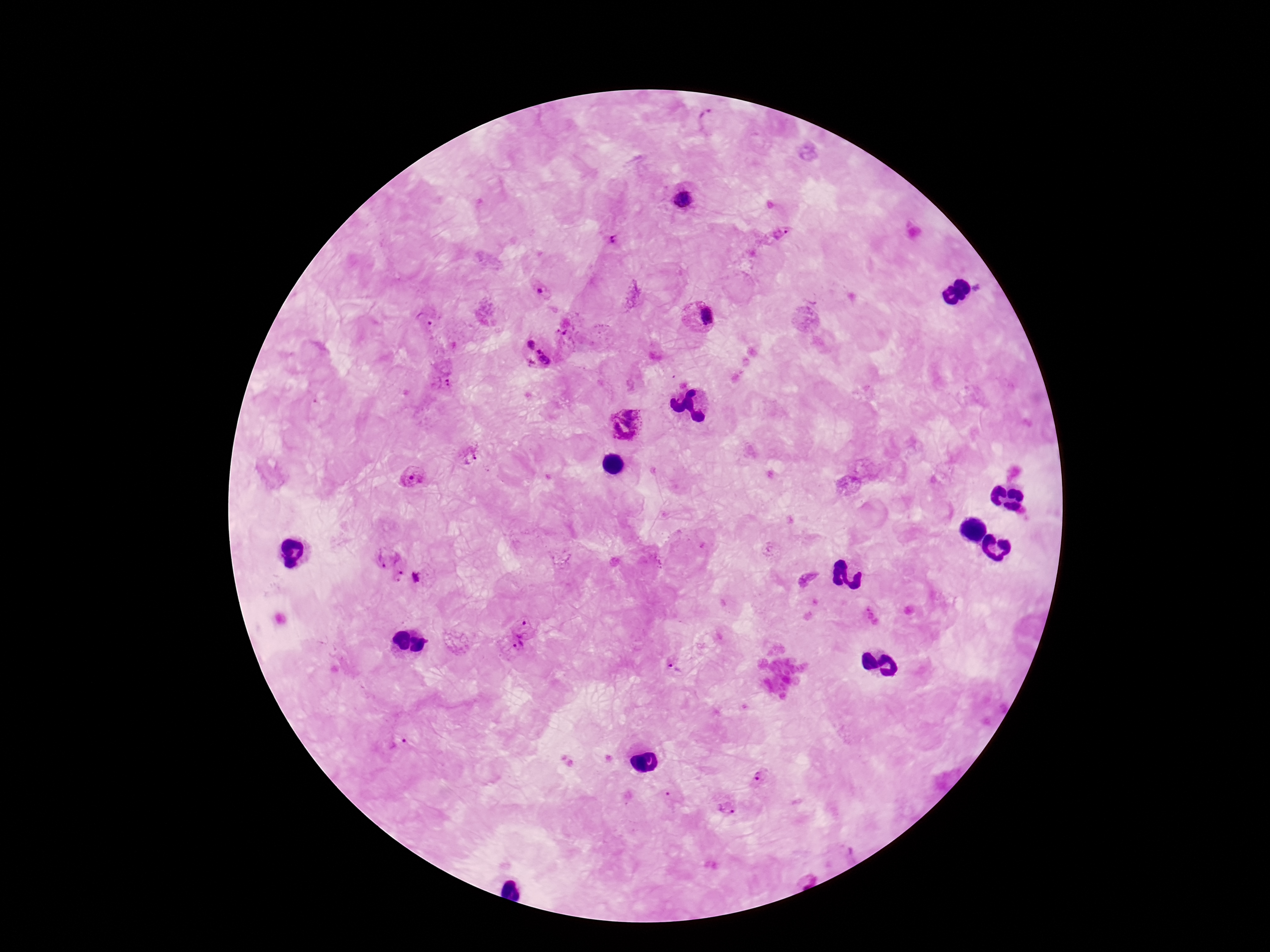
Approximate centers as {x, y} in pixels. Plasmodium parasite locations: {708, 119}, {682, 198}, {780, 233}, {616, 239}, {541, 291}, {699, 316}, {425, 320}, {564, 335}, {530, 344}, {540, 361}, {442, 383}, {626, 425}, {471, 456}, {411, 476}, {386, 556}, {399, 576}, {418, 579}, {872, 616}, {526, 623}, {512, 646}, {674, 667}, {402, 737}, {759, 776}, {671, 796}, {727, 807}. Giemsa-stained preparation. Patient malaria status: positive. Single field of view. 100x magnification. Image is 1270×952 pixels. Thick peripheral-blood smear. Photographed through the microscope eyepiece with a smartphone camera.